Give the extent of all Plasmodium ovale-infected red blood cells.
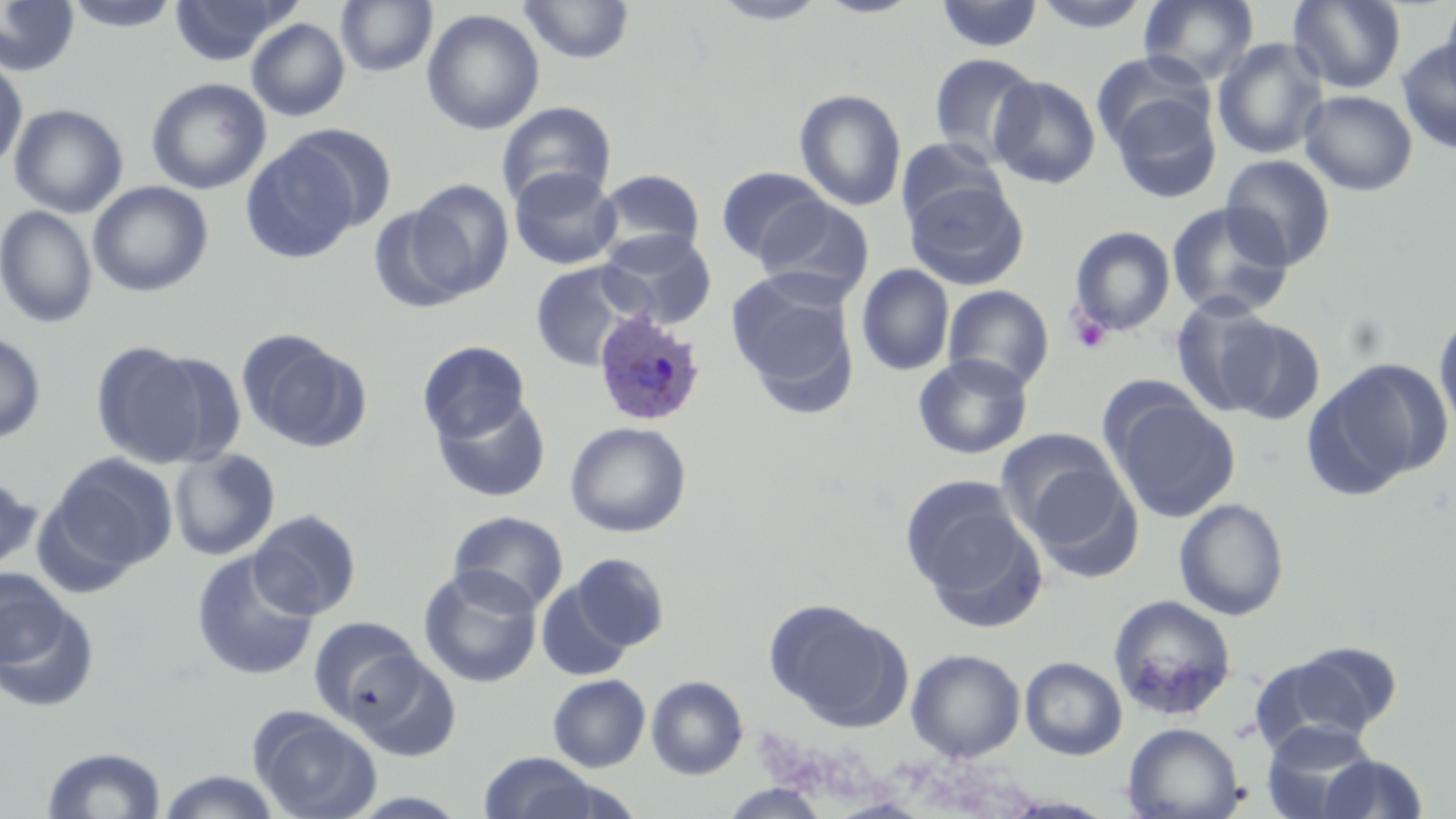

Approximate bounding boxes as (x1, y1, x2, y2) in pixels.
Plasmodium ovale-infected red blood cells: (592, 309, 709, 428).

Platelet locations: (1067, 309, 1113, 355). Uninfected red blood cell locations: (62, 0, 182, 33), (169, 0, 297, 66), (518, 0, 636, 64), (812, 0, 928, 19), (1030, 0, 1151, 34), (1137, 0, 1259, 85), (0, 1, 80, 77), (335, 1, 437, 78), (709, 1, 828, 26), (935, 1, 1044, 53), (1288, 1, 1407, 94), (1438, 1, 1456, 104), (421, 9, 545, 136), (246, 18, 349, 122), (1212, 38, 1329, 160), (1396, 39, 1456, 156), (1092, 50, 1215, 153), (928, 53, 1041, 165), (0, 56, 27, 173), (988, 75, 1101, 189), (146, 77, 271, 195), (794, 89, 907, 212), (1299, 89, 1418, 197), (1109, 91, 1222, 204), (495, 101, 617, 209), (8, 103, 128, 218), (288, 124, 399, 234), (895, 136, 1010, 233), (240, 142, 359, 264), (1220, 154, 1337, 270), (715, 166, 830, 264), (508, 167, 621, 270), (594, 169, 706, 260), (406, 179, 514, 299), (87, 181, 214, 298), (906, 181, 1029, 290), (755, 195, 875, 301), (1166, 202, 1294, 319), (0, 206, 98, 328), (367, 206, 470, 313), (1069, 226, 1176, 336), (598, 229, 717, 330), (529, 260, 650, 371), (855, 264, 955, 377), (726, 269, 859, 400), (942, 285, 1055, 391), (1169, 295, 1282, 416), (1434, 311, 1456, 437), (1220, 318, 1326, 423), (0, 331, 46, 444), (238, 331, 370, 453), (417, 340, 531, 443), (90, 341, 210, 468), (144, 351, 246, 468), (913, 353, 1034, 459), (1305, 357, 1452, 497), (1107, 392, 1241, 524), (431, 393, 552, 503), (565, 421, 691, 538), (996, 427, 1131, 551), (168, 449, 280, 561), (49, 453, 178, 573), (0, 473, 42, 574), (900, 474, 1038, 612), (1173, 498, 1289, 621), (248, 509, 362, 620), (447, 511, 568, 614), (190, 550, 319, 681), (569, 553, 670, 652), (418, 565, 543, 688), (0, 568, 73, 671), (536, 579, 634, 682), (1, 593, 100, 714), (1108, 595, 1237, 721), (767, 599, 910, 731), (309, 617, 424, 722), (1253, 644, 1399, 750), (345, 648, 461, 761), (906, 648, 1025, 762), (1020, 656, 1127, 760), (547, 674, 650, 772), (646, 675, 748, 780), (252, 712, 381, 819), (1260, 720, 1380, 818), (1122, 722, 1244, 819), (40, 745, 168, 818), (478, 752, 602, 819), (1317, 754, 1430, 818), (155, 770, 285, 819), (717, 783, 831, 818). Slide-level diagnosis: Plasmodium ovale. Image is 1456×819 pixels. May-Grünwald-Giemsa stain. One field of a larger specimen. 1000x magnification. Light microscopy. Thin blood film.